Locate every blood parasite and identify its species.
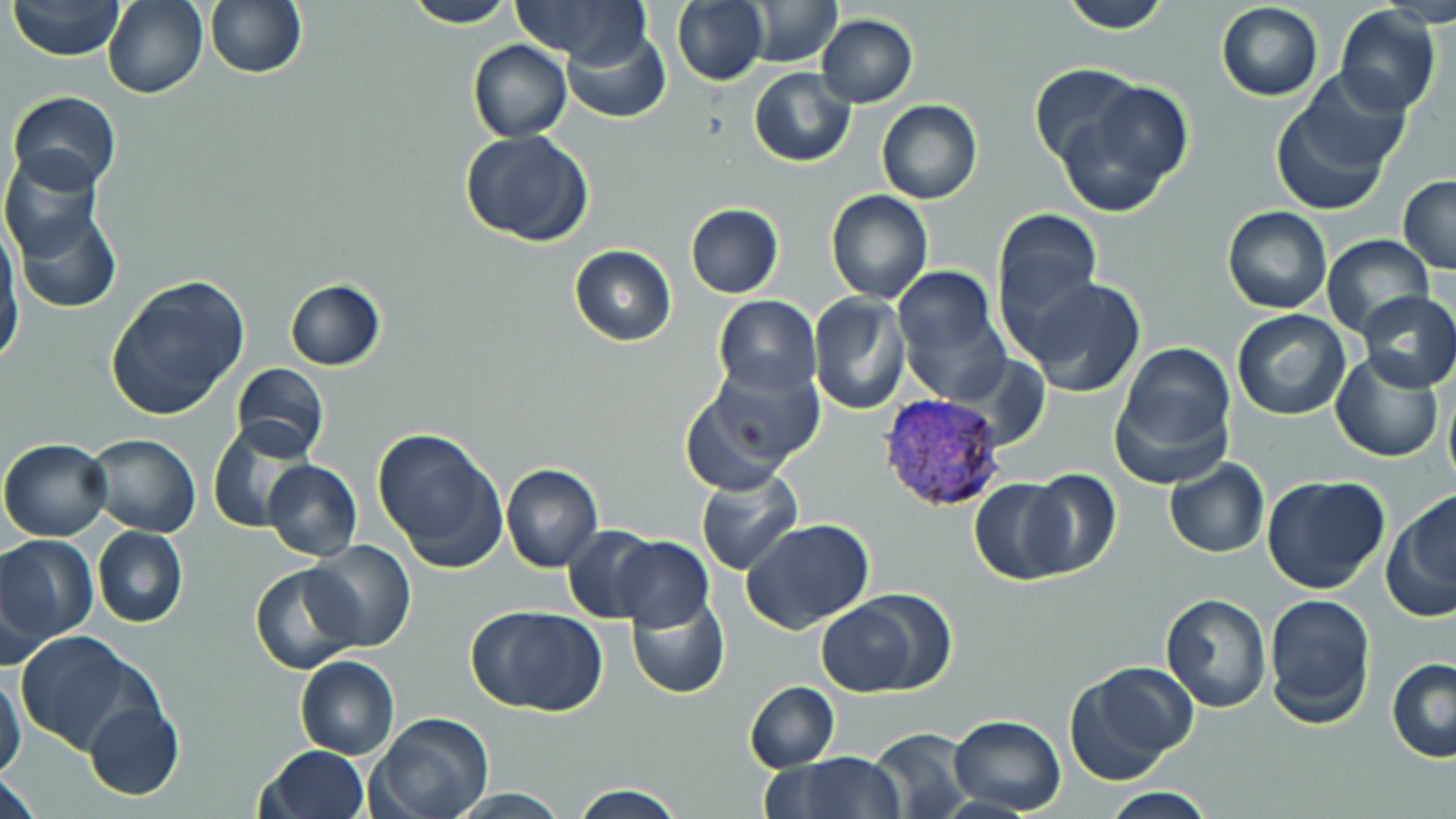
Approximate bounding boxes as (x1,y1)-(x2,y2) corner pairs in pixels.
Plasmodium vivax-infected red blood cells: (878,393)-(1005,513).
No Plasmodium falciparum, Plasmodium ovale, Plasmodium malariae, Babesia divergens, or Trypanosoma brucei observed.

Summary:
  - Uninfected red blood cell locations: (7,0)-(127,60), (103,0)-(208,99), (205,0)-(307,80), (508,0)-(647,62), (672,0)-(768,85), (742,0)-(842,67), (1059,0)-(1172,33), (399,1)-(521,27), (1215,2)-(1323,101), (1335,6)-(1441,116), (816,14)-(918,107), (561,25)-(670,124), (467,39)-(571,142), (1028,65)-(1141,169), (749,68)-(856,167), (1074,78)-(1193,204), (1272,85)-(1404,217), (7,90)-(122,192), (876,99)-(983,204), (459,129)-(594,247), (3,154)-(116,310), (1398,176)-(1456,273), (825,190)-(932,303), (685,203)-(783,299), (1222,206)-(1332,314), (992,209)-(1104,324), (1,232)-(23,366), (1322,235)-(1433,339), (569,245)-(676,345), (106,276)-(250,421), (1021,276)-(1147,398), (283,279)-(386,371), (896,285)-(1012,406), (1355,290)-(1456,391), (807,293)-(910,415), (713,295)-(820,395), (1231,309)-(1352,422), (1112,342)-(1235,477), (1332,352)-(1442,462), (232,363)-(329,461), (683,367)-(821,487), (1442,379)-(1456,493), (209,424)-(309,532), (372,425)-(508,571), (84,433)-(201,537), (1,437)-(113,542), (1164,458)-(1269,559), (263,460)-(361,560), (501,463)-(603,571), (695,469)-(804,574), (1020,469)-(1123,578), (1262,473)-(1391,595), (969,478)-(1075,584), (1382,494)-(1456,625), (741,518)-(875,636), (563,524)-(667,624), (93,527)-(187,628), (0,532)-(96,653), (607,536)-(714,632), (304,540)-(416,653), (251,564)-(361,674), (624,591)-(730,700), (1263,591)-(1376,728), (1159,594)-(1271,713), (816,601)-(922,696), (467,605)-(609,715), (16,632)-(153,757), (295,655)-(399,759), (1387,657)-(1456,763), (1063,662)-(1195,785), (0,672)-(27,779), (743,681)-(839,772), (82,699)-(183,801), (368,713)-(492,819), (947,715)-(1067,816), (868,728)-(975,818), (256,745)-(369,819), (767,752)-(907,818), (1,768)-(43,819), (568,783)-(687,817), (1100,787)-(1218,819), (449,789)-(574,819)
  - Slide-level diagnosis: Plasmodium vivax
  - Preparation: thin blood film
  - Magnification: 1000x
  - Field of view: single
  - Stain: May-Grünwald-Giemsa
  - Modality: optical microscopy
  - Image size: 1456×819 pixels